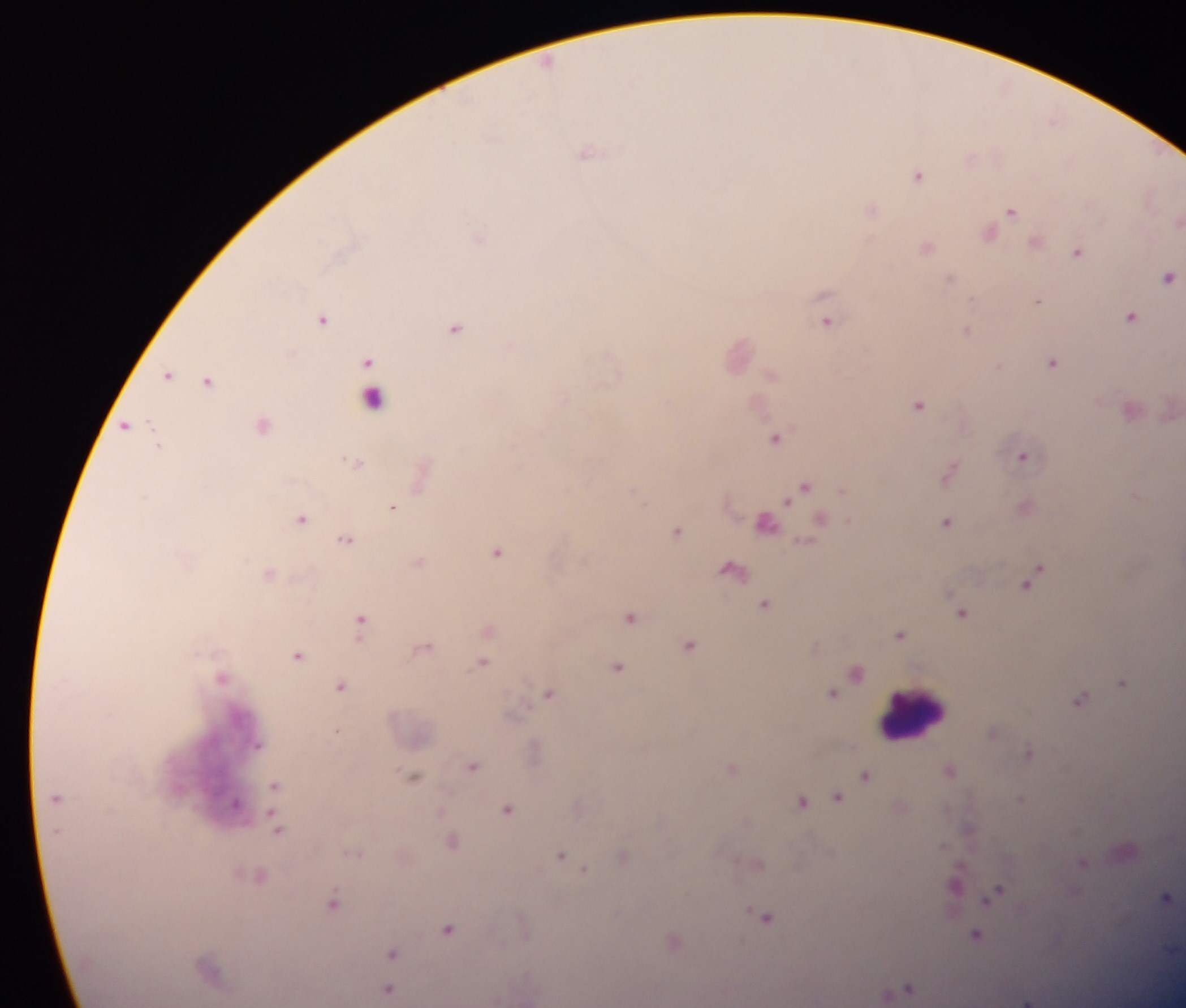

Approximate centers as x y in pixels. Leukocyte locations: 914 713. Plasmodium parasite locations: 1053 122; 588 152; 972 159; 919 175; 872 209; 1012 210; 990 233; 1036 241; 928 247; 1078 252; 949 278; 1168 278; 1038 301; 1131 317; 323 319; 827 322; 456 328; 967 331; 368 360; 1052 362; 169 375; 772 375; 208 381; 373 398; 918 404; 125 425; 776 438; 1022 457; 358 463; 949 472; 804 488; 393 506; 301 519; 821 521; 767 522; 947 522; 678 532; 346 539; 497 552; 731 569; 1033 579; 766 605; 962 614; 631 618; 361 621; 901 634; 690 646; 298 656; 483 662; 618 667; 857 673; 1124 682; 341 685; 549 693; 833 695; 1080 700; 1028 754; 473 767; 733 769; 950 771; 414 776; 866 776; 275 785; 839 797; 1021 800; 801 802; 237 803; 508 810; 277 829; 452 843; 562 856; 623 857; 1083 863; 583 869; 956 883; 996 893; 1166 897; 333 903; 767 918; 448 929; 976 936; 674 943; 393 953; 909 989; 389 990; 1027 1001. Photographed through a microscope with a mobile-phone camera. Image is 1186×1008 pixels. Sample from Ghana. Thick blood smear. Single field of view.